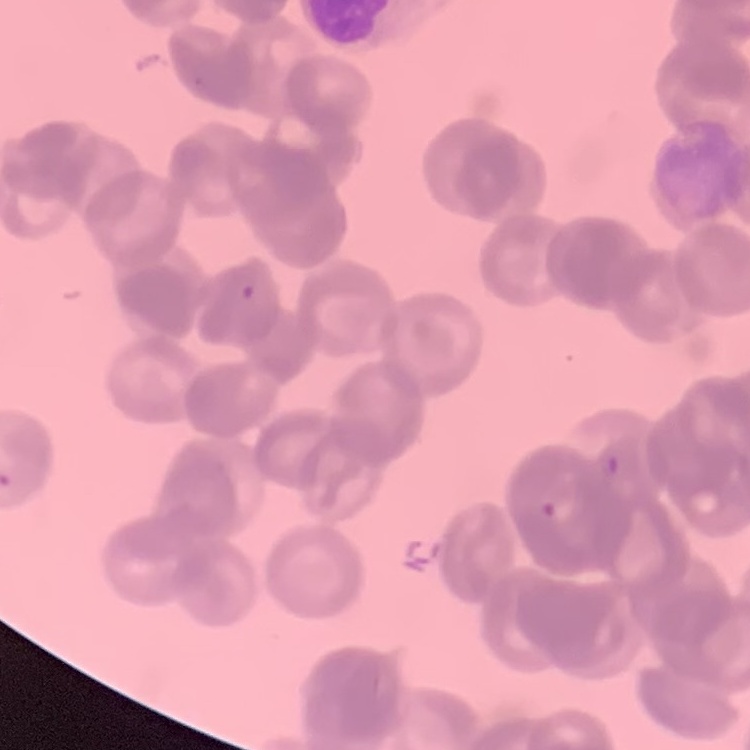
{
  "red_blood_cell_morphology": "rouleaux formation",
  "stain": "Field's or Giemsa",
  "image_type": "one tile cut from a larger photomicrograph",
  "preparation": "thin blood smear"
}